State the blood parasite species.
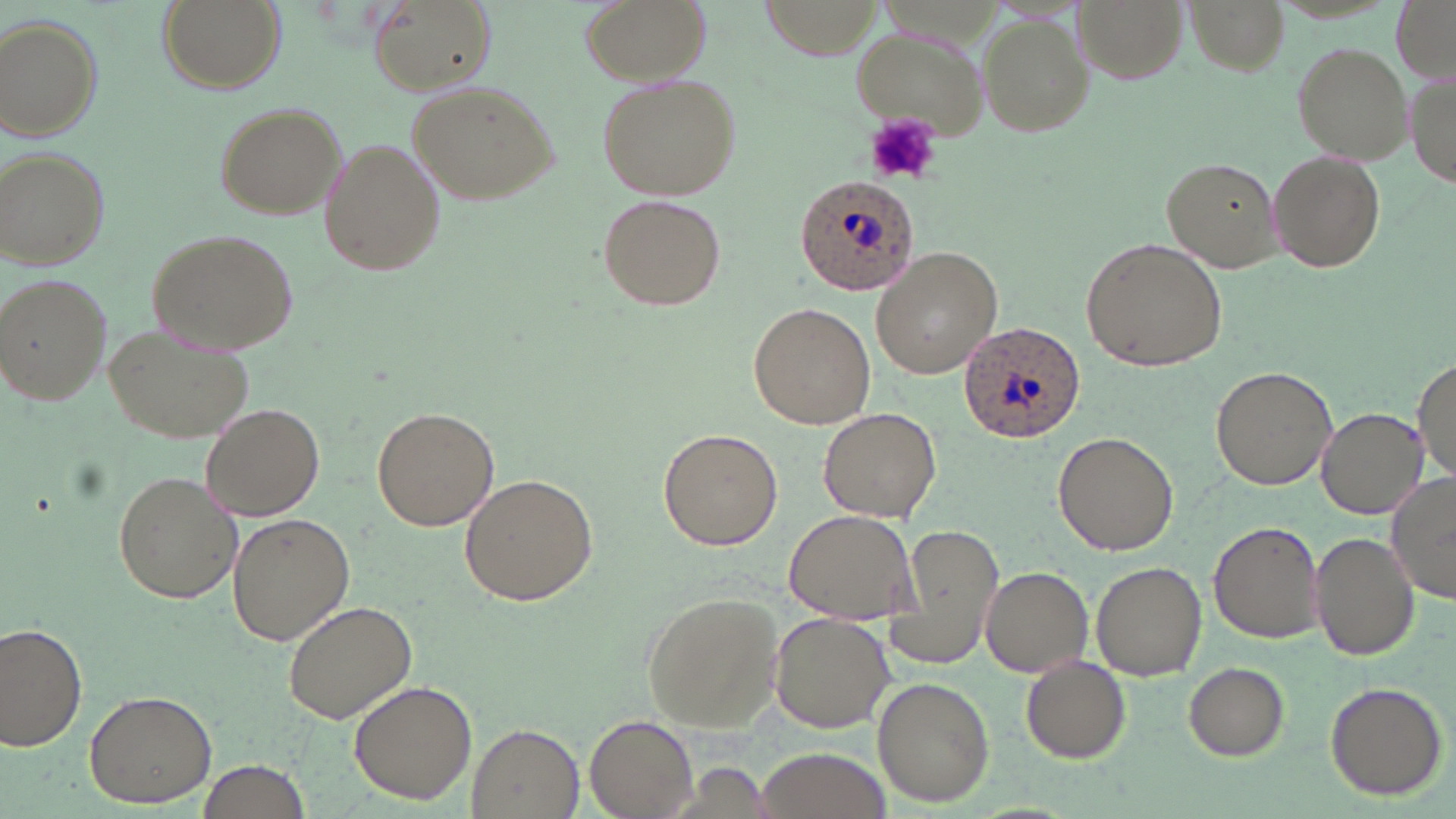
Plasmodium ovale.

{
  "modality": "light microscopy",
  "uninfected_red_blood_cell_locations": "approximate bounding boxes as (x1,y1)-(x2,y2) corner pairs in pixels: (158,0)-(286,96), (580,0)-(709,87), (1072,0)-(1187,84), (1185,0)-(1289,74), (1389,0)-(1456,81), (369,1)-(494,97), (979,10)-(1096,134), (2,15)-(104,143), (847,23)-(989,144), (1290,40)-(1413,167), (1408,70)-(1455,193), (595,72)-(741,200), (409,78)-(559,206), (210,101)-(346,221), (318,137)-(445,280), (0,144)-(110,270), (1265,147)-(1388,273), (1161,157)-(1283,273), (599,194)-(726,311), (145,228)-(300,356), (1081,236)-(1227,372), (870,247)-(1003,379), (0,271)-(111,404), (748,302)-(876,429), (100,320)-(254,445), (1415,356)-(1454,485), (1211,365)-(1337,490), (201,401)-(326,521), (372,406)-(499,532), (817,406)-(944,523), (1318,408)-(1427,518), (657,428)-(783,551), (1053,431)-(1179,555), (113,470)-(243,605), (460,473)-(598,609), (1387,473)-(1456,605), (782,508)-(920,625), (227,512)-(355,647), (1208,520)-(1324,645), (884,522)-(1004,667), (1310,532)-(1420,662), (1093,562)-(1206,681), (979,565)-(1094,679), (641,591)-(786,732), (283,601)-(419,724), (768,611)-(895,734), (0,622)-(90,753), (1021,654)-(1132,764), (1184,661)-(1292,760), (872,677)-(995,807), (1322,679)-(1449,800), (348,681)-(476,804), (83,689)-(217,809), (584,712)-(700,818), (465,724)-(584,819), (754,746)-(889,819), (194,757)-(313,819)",
  "field_of_view": "one of a larger specimen",
  "magnification": "1000x",
  "plasmodium_ovale_infected_red_blood_cell_locations": "approximate bounding boxes as (x1,y1)-(x2,y2) corner pairs in pixels: (793,173)-(918,298), (958,321)-(1087,441)",
  "preparation": "thin blood film",
  "image_size": "1456×819 pixels",
  "platelet_locations": "approximate bounding boxes as (x1,y1)-(x2,y2) corner pairs in pixels: (866,112)-(940,186)",
  "stain": "May-Grünwald-Giemsa"
}